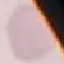

Summary:
  - Result: no malaria parasites detected
  - Capture: smartphone camera at the microscope eyepiece
  - Stain: Giemsa
  - Image type: automatically extracted cell patch, resized to 64 × 64 pixels
  - Preparation: thin blood film